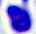

{
  "identification": "white blood cell",
  "modality": "photomicrograph",
  "magnification": "400x"
}